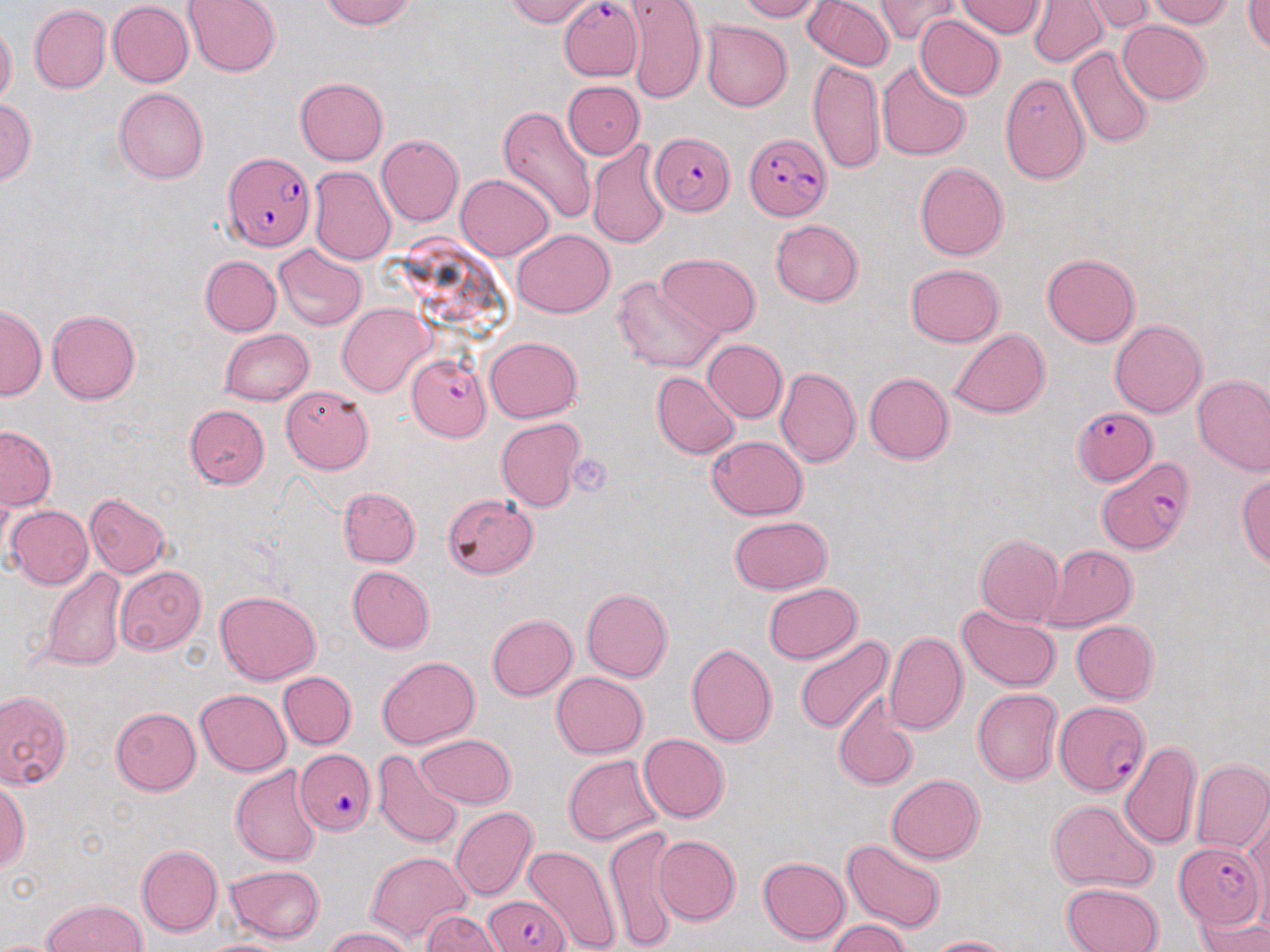
slide_level_diagnosis: Plasmodium falciparum
platelet_locations: 'approximate bounding boxes as (x1, y1, x2, y2) in pixels: (571, 452, 613, 497)'
uninfected_red_blood_cell_locations: 'approximate bounding boxes as (x1, y1, x2, y2) in pixels: (182, 0, 281, 77), (320, 0, 415, 29), (505, 0, 596, 24), (624, 0, 705, 103), (737, 0, 824, 22), (803, 0, 894, 71), (1029, 0, 1107, 68), (1079, 0, 1158, 33), (1146, 0, 1233, 27), (1244, 0, 1270, 54), (107, 1, 193, 87), (876, 1, 959, 43), (954, 1, 1046, 39), (28, 3, 111, 93), (915, 16, 1005, 100), (701, 18, 792, 111), (1118, 20, 1210, 104), (0, 22, 17, 108), (1066, 46, 1155, 149), (807, 59, 886, 174), (877, 61, 972, 160), (999, 72, 1089, 184), (295, 77, 388, 165), (562, 81, 644, 159), (114, 87, 209, 184), (1, 97, 36, 187), (500, 105, 598, 224), (376, 134, 464, 226), (586, 138, 669, 250), (914, 162, 1009, 260), (309, 166, 397, 265), (455, 174, 553, 261), (770, 219, 863, 306), (513, 229, 614, 317), (274, 244, 366, 330), (656, 252, 761, 337), (1041, 253, 1141, 346), (200, 255, 281, 336), (905, 264, 1004, 347), (612, 277, 725, 374), (338, 303, 435, 398), (0, 305, 46, 401), (47, 310, 140, 404), (1110, 319, 1207, 417), (948, 328, 1050, 419), (220, 329, 314, 406), (484, 336, 582, 421), (702, 339, 787, 421), (774, 367, 861, 468), (651, 372, 739, 459), (863, 372, 955, 464), (1193, 373, 1270, 474), (280, 386, 374, 473), (183, 405, 269, 489), (497, 417, 587, 512), (0, 425, 56, 510), (705, 436, 809, 519), (1235, 472, 1270, 569), (0, 482, 15, 572), (338, 486, 420, 567), (85, 493, 171, 578), (442, 494, 538, 579), (7, 505, 94, 589), (728, 515, 833, 595), (975, 534, 1064, 625), (1043, 544, 1138, 631), (114, 566, 206, 655), (347, 566, 435, 653), (43, 568, 127, 672), (763, 584, 863, 664), (581, 587, 673, 682), (216, 590, 321, 684), (956, 605, 1061, 691), (487, 614, 577, 700), (1071, 620, 1160, 703), (884, 631, 967, 734), (794, 634, 894, 734), (685, 642, 777, 748), (377, 655, 481, 749), (278, 672, 356, 749), (551, 672, 648, 757), (972, 688, 1063, 784), (195, 689, 291, 776), (0, 690, 73, 787), (833, 694, 919, 791), (110, 707, 202, 795), (638, 733, 729, 822), (415, 734, 516, 809), (1118, 740, 1201, 849), (372, 749, 465, 849), (563, 753, 663, 845), (1190, 758, 1270, 854), (231, 765, 325, 866), (886, 773, 984, 864), (0, 780, 29, 872), (1047, 800, 1159, 893), (451, 807, 538, 901), (604, 825, 683, 950), (652, 834, 741, 926), (842, 838, 947, 932), (136, 844, 222, 937), (521, 845, 621, 951), (365, 850, 472, 943), (758, 856, 851, 945), (225, 864, 325, 943), (1062, 882, 1164, 952), (41, 899, 145, 952), (423, 910, 504, 952), (1194, 910, 1270, 952), (825, 919, 911, 952), (324, 927, 412, 952), (925, 936, 1017, 952), (0, 938, 59, 952), (195, 938, 293, 952)'
field_of_view: single
modality: optical microscopy
stain: May-Grünwald-Giemsa
plasmodium_falciparum_infected_red_blood_cell_locations: 'approximate bounding boxes as (x1, y1, x2, y2) in pixels: (558, 0, 642, 81), (648, 131, 736, 215), (743, 131, 831, 220), (222, 153, 313, 252), (407, 355, 491, 441), (1070, 405, 1158, 487), (1093, 457, 1197, 554), (1054, 701, 1150, 795), (296, 748, 376, 834), (1176, 840, 1262, 929), (484, 894, 568, 951)'
magnification: 1000x
preparation: thin blood smear
image_size: 1270×952 pixels